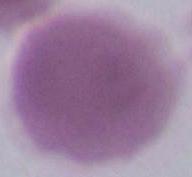
Summary:
  - Magnification: 1000x
  - Modality: photomicrograph
  - Identification: red blood cell